Assess this cell for malaria.
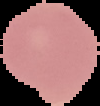

Uninfected.

From a thin blood smear. Image is 100×106 pixels. Segmented cell region on a black background.